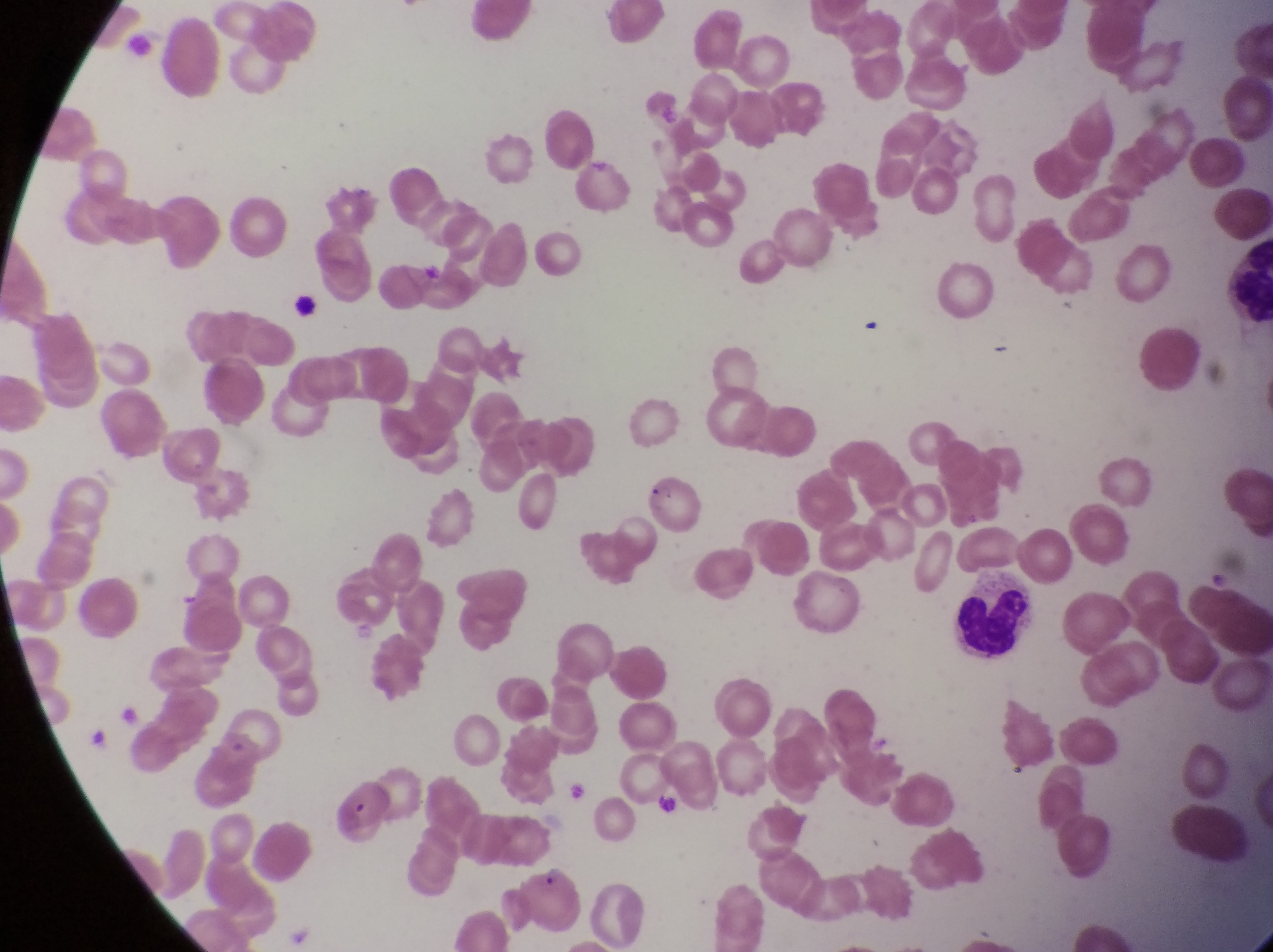

preparation = thin blood smear
leukocyte locations = approximate bounding boxes as [left, top, right, bottom] in pixels: [958, 575, 1043, 672]
image size = 1273×952 pixels
country = Uganda
field of view = single
magnification = 1000x
capture = smartphone photograph through the eyepiece of an Olympus CX-23 microscope
parasitised red blood cell locations = approximate bounding boxes as [left, top, right, bottom] in pixels: [637, 470, 702, 538], [522, 856, 585, 936]